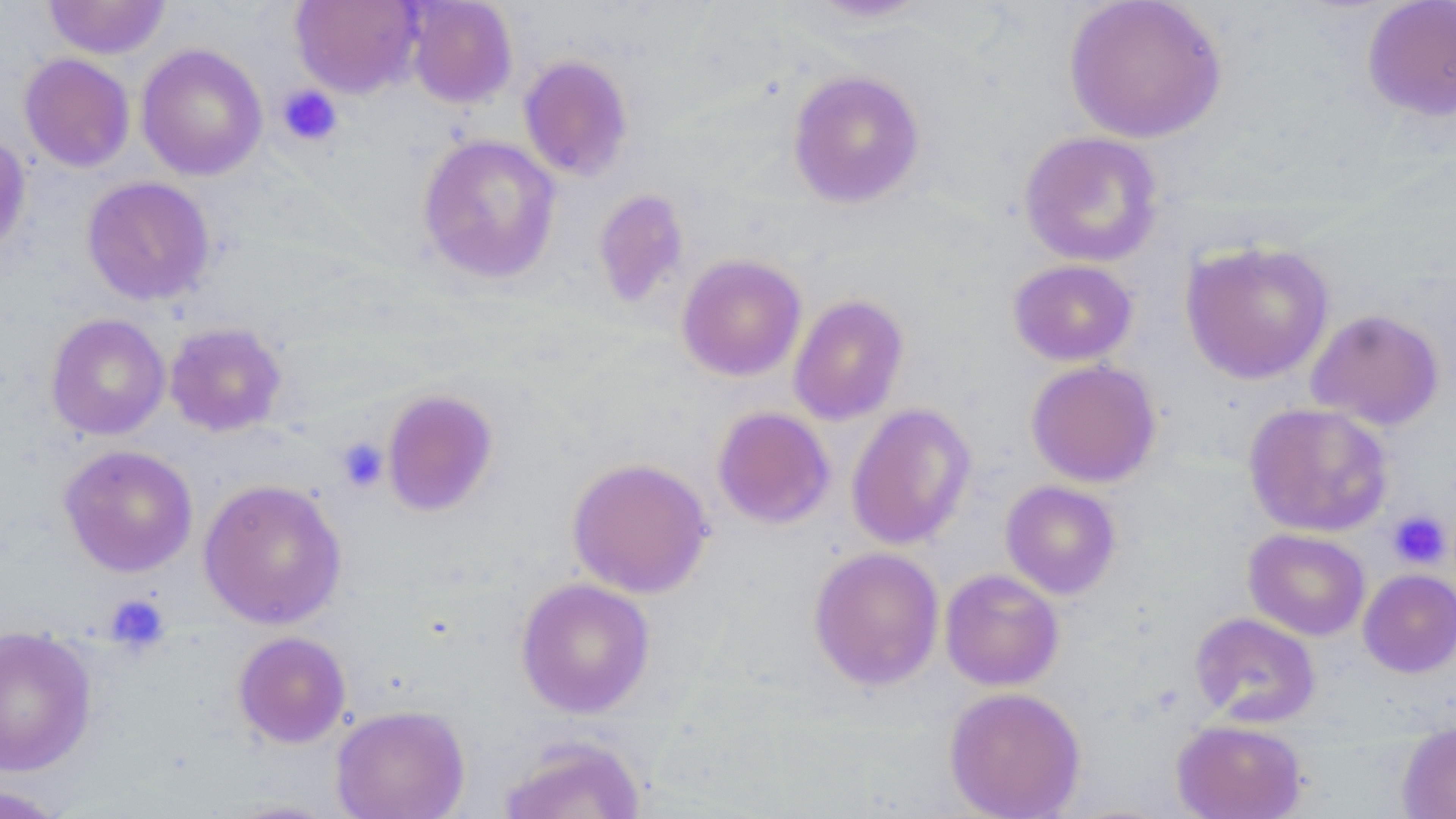

Approximate bounding boxes as [x1, y1, x2, y2] in pixels. Platelet locations: [277, 84, 343, 147], [335, 437, 389, 492], [1387, 510, 1453, 568], [104, 593, 170, 655]. Uninfected red blood cell locations: [405, 0, 518, 109], [795, 0, 939, 25], [1063, 0, 1228, 144], [43, 1, 171, 59], [290, 1, 423, 99], [1361, 1, 1456, 122], [136, 44, 267, 181], [19, 53, 135, 172], [518, 55, 635, 181], [787, 69, 925, 208], [1019, 130, 1165, 267], [0, 131, 31, 258], [417, 134, 561, 284], [81, 176, 215, 306], [592, 188, 691, 310], [1181, 240, 1334, 385], [676, 253, 807, 382], [1008, 259, 1138, 366], [788, 294, 909, 426], [1306, 308, 1445, 431], [45, 313, 170, 441], [164, 321, 288, 437], [1025, 359, 1162, 488], [380, 388, 499, 517], [1243, 401, 1393, 538], [846, 403, 977, 551], [712, 406, 836, 529], [58, 444, 198, 577], [567, 456, 713, 599], [198, 478, 347, 630], [1000, 480, 1122, 599], [1243, 529, 1371, 641], [808, 546, 945, 691], [940, 568, 1064, 691], [1358, 569, 1456, 678], [515, 577, 655, 718], [1190, 612, 1321, 727], [1, 626, 97, 777], [232, 631, 351, 748], [943, 686, 1086, 819], [331, 704, 470, 819], [1172, 719, 1308, 819], [1397, 722, 1456, 819], [497, 735, 648, 819], [0, 784, 70, 818], [214, 798, 345, 818]. Slide-level diagnosis: no evidence of blood parasites. Image is 1456×819 pixels. Thin blood film. Light microscopy. Single field of view. May-Grünwald-Giemsa-stained preparation. 1000x magnification.